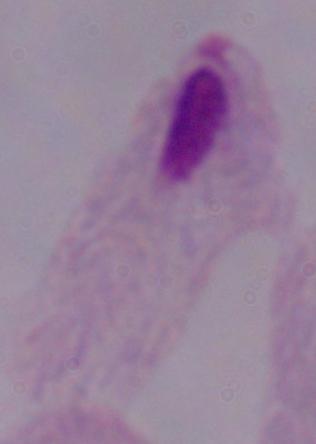
magnification = 1000x
modality = photomicrograph
identification = trichomonad